Name the parasite shown.
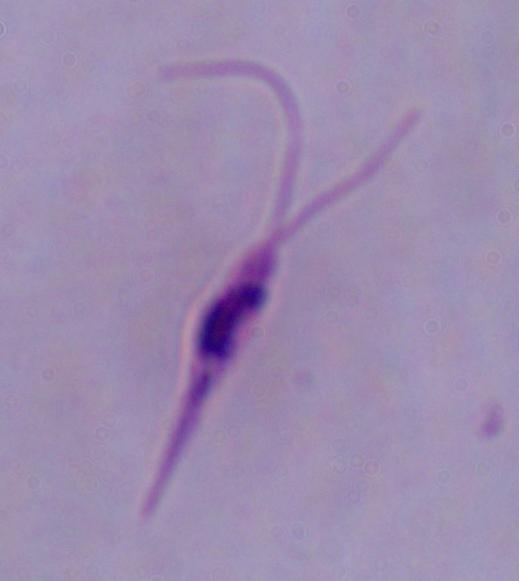
Leishmania.

Photomicrograph. 1000x magnification.